Assess this cell for malaria.
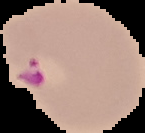

It is parasitized.

{
  "image_type": "segmented cell region on a black background",
  "preparation": "thin blood film",
  "image_size": "145×133 pixels"
}